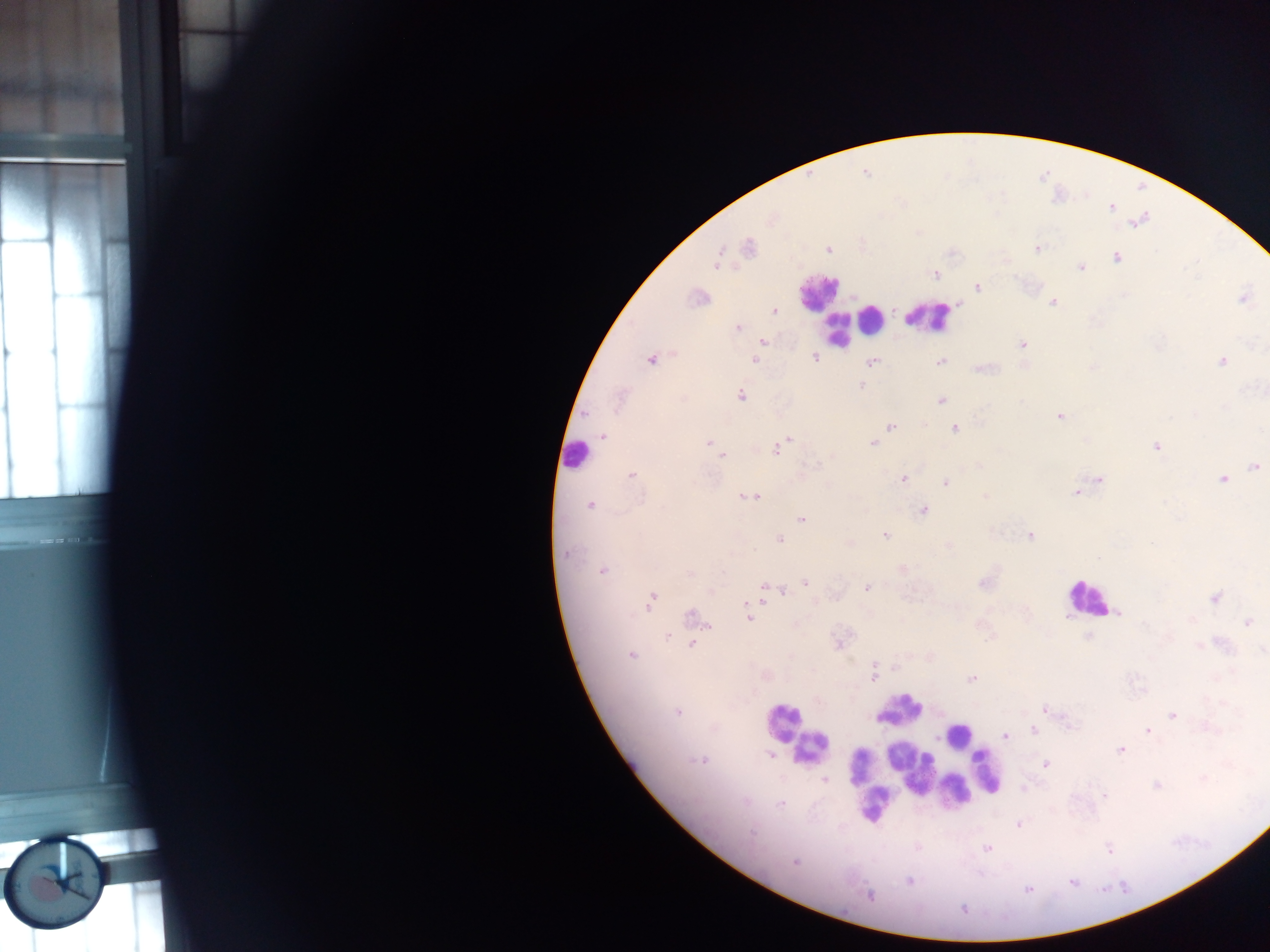
Approximate centers as [x, y] in pixels. Leukocyte locations: [818, 293], [929, 316], [873, 320], [849, 323], [837, 331], [576, 456], [1087, 597], [899, 710], [783, 722], [958, 734], [811, 748], [889, 754], [911, 762], [858, 766], [864, 769], [986, 771], [935, 775], [954, 790], [875, 803]. Plasmodium parasite locations: [748, 248], [1036, 248], [827, 249], [1116, 257], [716, 260], [1081, 266], [935, 274], [977, 287], [697, 297], [1242, 297], [1052, 302], [773, 310], [737, 328], [761, 342], [1021, 344], [815, 357], [651, 358], [755, 360], [1222, 360], [871, 361], [939, 361], [979, 368], [863, 383], [860, 385], [740, 395], [941, 400], [1059, 415], [890, 427], [955, 428], [602, 436], [787, 438], [708, 442], [873, 442], [1156, 446], [715, 447], [775, 448], [722, 455], [1255, 466], [632, 474], [903, 479], [1099, 479], [1223, 479], [946, 482], [1077, 492], [756, 495], [747, 497], [589, 504], [923, 510], [801, 518], [884, 534], [1029, 535], [779, 539], [849, 542], [948, 546], [566, 554], [901, 568], [603, 570], [984, 581], [806, 582], [765, 586], [866, 588], [783, 591], [764, 594], [1215, 598], [651, 601], [1118, 613], [691, 617], [748, 617], [1248, 622], [1088, 638], [839, 642], [691, 644], [1200, 645], [631, 655], [873, 673], [971, 679], [1045, 708], [677, 711], [1172, 716], [1034, 730], [1148, 730], [1005, 736], [1122, 749], [772, 755], [700, 759], [1046, 763], [824, 780], [1155, 786], [1105, 796], [780, 804], [1019, 824], [917, 847], [987, 848], [1109, 850], [795, 862], [909, 881], [1027, 889], [870, 896], [964, 909]. Mobile-phone photograph taken through the microscope. Thick blood smear. One field of view. Sample from Ghana. Image is 1270×952 pixels.